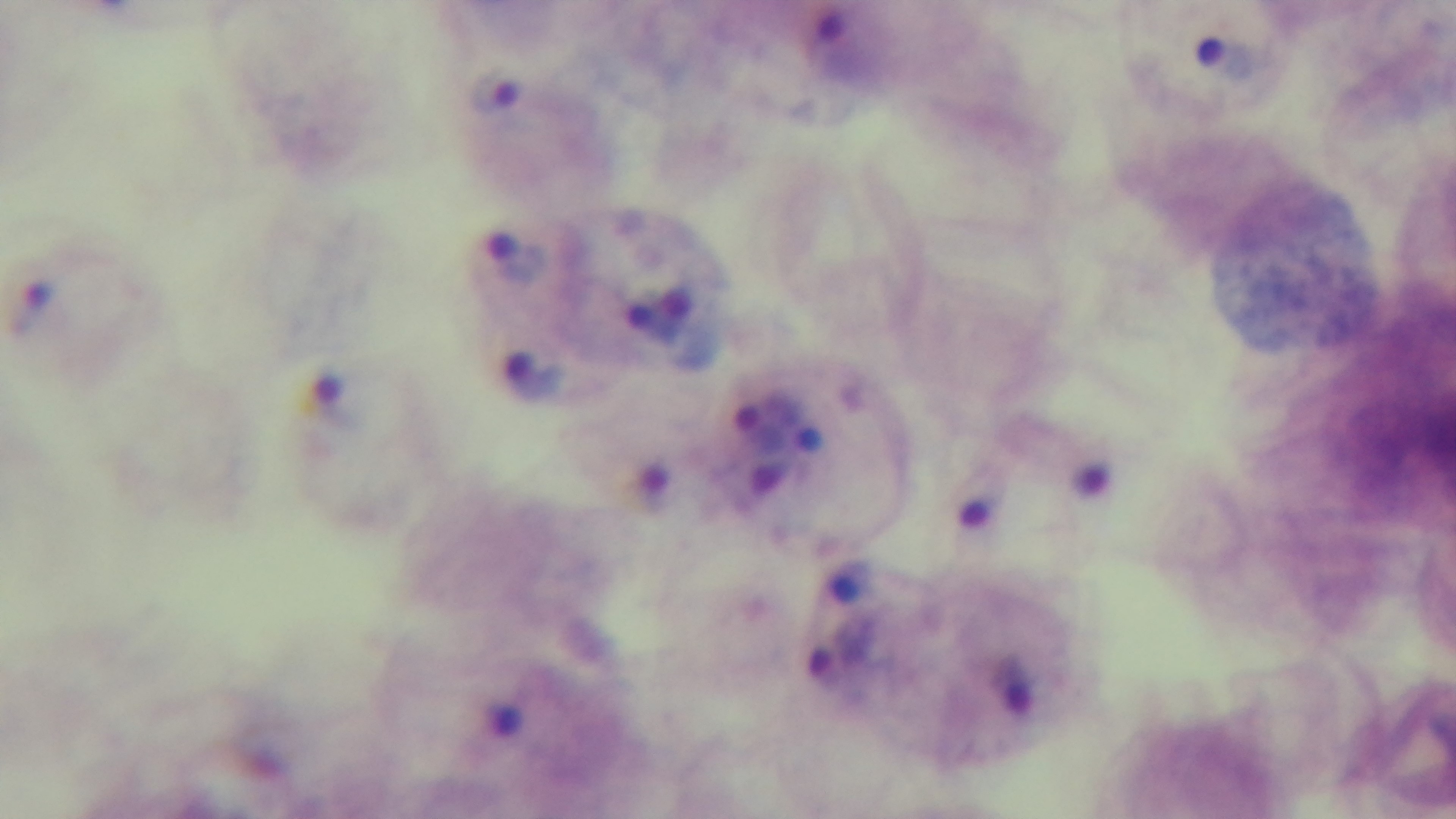

Summary:
  - Objective: 100x oil immersion
  - Field of view: one from the slide
  - Capture: mounted 4K digital camera
  - Stain: Giemsa
  - Modality: light microscopy
  - Preparation: thick
  - Malaria status: positive